Identify the blood parasite species.
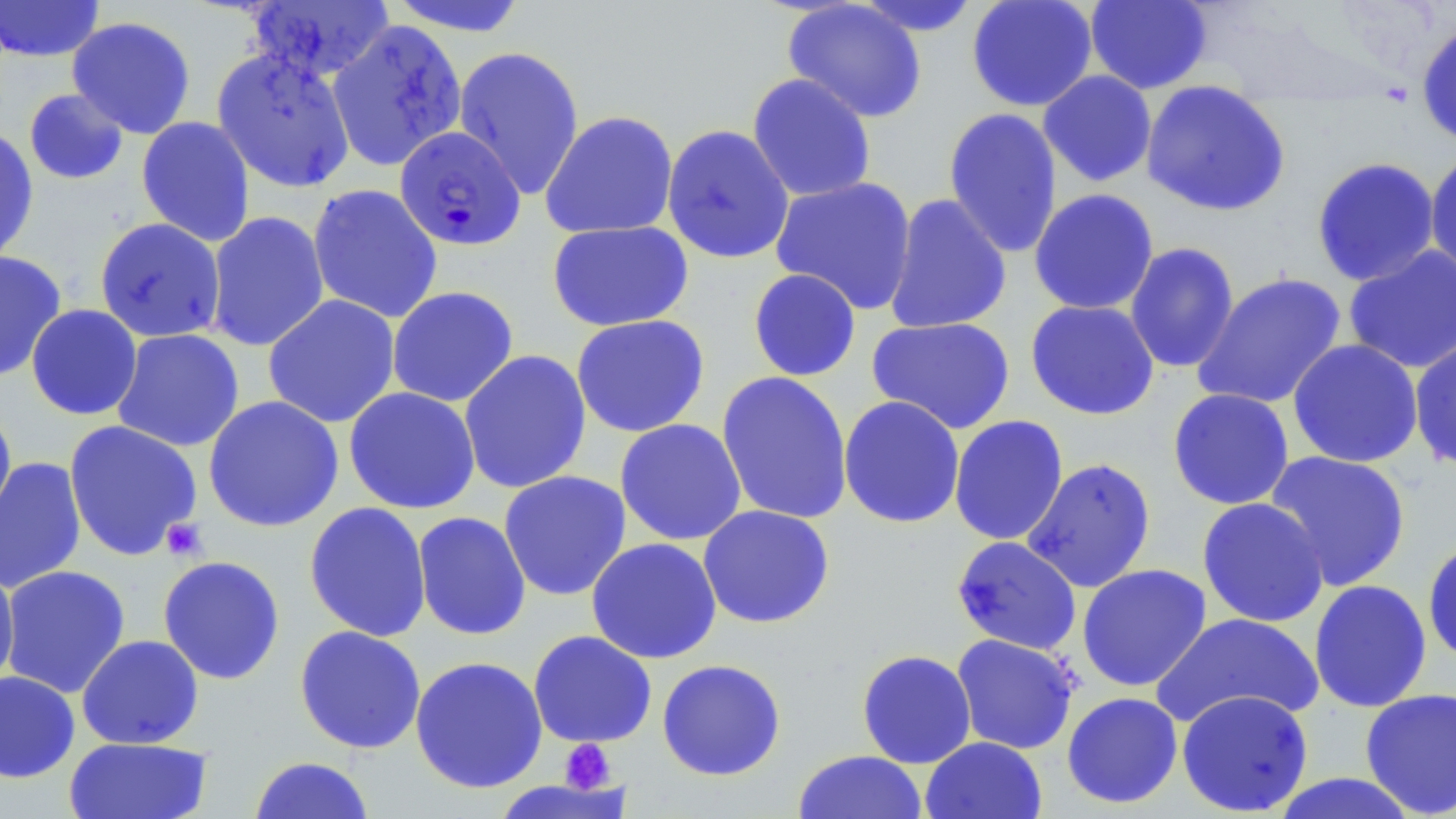

Plasmodium falciparum.

Approximate bounding boxes as (x1, y1, x2, y2) in pixels. Uninfected red blood cell locations: (386, 0, 532, 37), (851, 0, 984, 38), (966, 0, 1098, 112), (1084, 0, 1213, 94), (1, 1, 105, 62), (245, 1, 395, 82), (782, 1, 928, 123), (67, 16, 197, 139), (328, 20, 467, 171), (1415, 22, 1456, 147), (453, 46, 585, 200), (212, 48, 356, 193), (1038, 70, 1158, 188), (747, 73, 876, 203), (1141, 80, 1291, 218), (23, 88, 130, 185), (942, 106, 1063, 258), (540, 110, 679, 240), (136, 116, 256, 246), (661, 124, 795, 264), (0, 127, 39, 265), (1425, 147, 1456, 281), (1311, 157, 1441, 286), (770, 176, 918, 315), (307, 184, 444, 324), (1028, 188, 1160, 315), (884, 193, 1012, 335), (205, 211, 330, 352), (94, 218, 226, 342), (547, 220, 695, 332), (1124, 242, 1240, 374), (1342, 245, 1456, 374), (0, 250, 67, 382), (748, 268, 861, 382), (1191, 271, 1347, 410), (386, 286, 519, 407), (263, 294, 401, 429), (1025, 299, 1160, 420), (26, 304, 142, 420), (570, 314, 710, 438), (866, 316, 1015, 435), (111, 328, 245, 452), (1409, 334, 1456, 473), (1287, 338, 1424, 468), (458, 349, 592, 494), (716, 371, 854, 525), (343, 386, 481, 514), (1167, 388, 1295, 510), (203, 395, 344, 532), (838, 395, 966, 529), (0, 404, 17, 530), (949, 415, 1069, 546), (614, 418, 747, 546), (63, 419, 203, 561), (1263, 450, 1412, 591), (0, 456, 87, 594), (1022, 457, 1157, 593), (498, 470, 632, 601), (1196, 497, 1329, 627), (304, 501, 432, 642), (697, 504, 835, 629), (412, 511, 531, 641), (1422, 535, 1456, 668), (951, 536, 1082, 654), (585, 537, 722, 664), (157, 555, 286, 685), (0, 563, 20, 689), (1077, 563, 1212, 692), (1, 565, 131, 698), (1308, 579, 1432, 713), (1151, 613, 1323, 729), (294, 625, 427, 754), (528, 630, 657, 748), (950, 633, 1080, 755), (76, 634, 204, 749), (856, 649, 977, 768), (409, 655, 548, 794), (656, 659, 787, 781), (0, 670, 80, 783), (1359, 687, 1456, 817), (1176, 690, 1314, 816), (1062, 691, 1183, 809), (64, 736, 213, 819), (920, 736, 1047, 819), (792, 750, 927, 819), (247, 756, 376, 818), (1269, 773, 1421, 818). Plasmodium falciparum-infected red blood cell locations: (395, 126, 525, 250). Platelet locations: (160, 518, 208, 561), (559, 738, 616, 793). May-Grünwald-Giemsa-stained preparation. Optical microscopy. Image is 1456×819 pixels. Single field of view. 1000x magnification. Thin blood film.